Assess this cell for malaria.
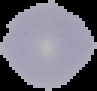
Uninfected.

Summary:
  - Image type: segmented cell region with the area outside set to black
  - Image size: 97×91 pixels
  - Preparation: thin blood film